Assess the morphology of the red blood cells.
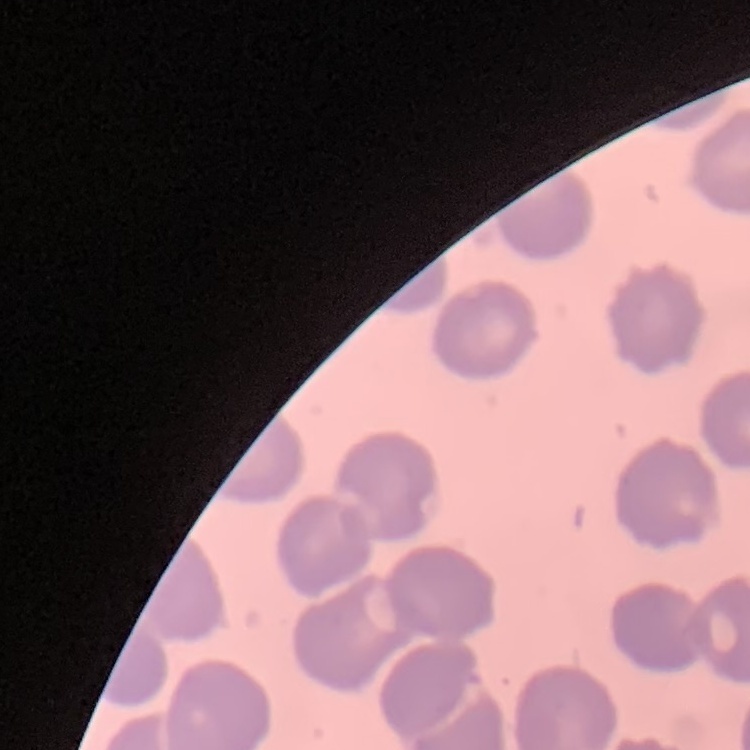
They show no rouleaux formation.

Stained with either Field's or Giemsa. Square crop of a larger photomicrograph. Thin peripheral smear.